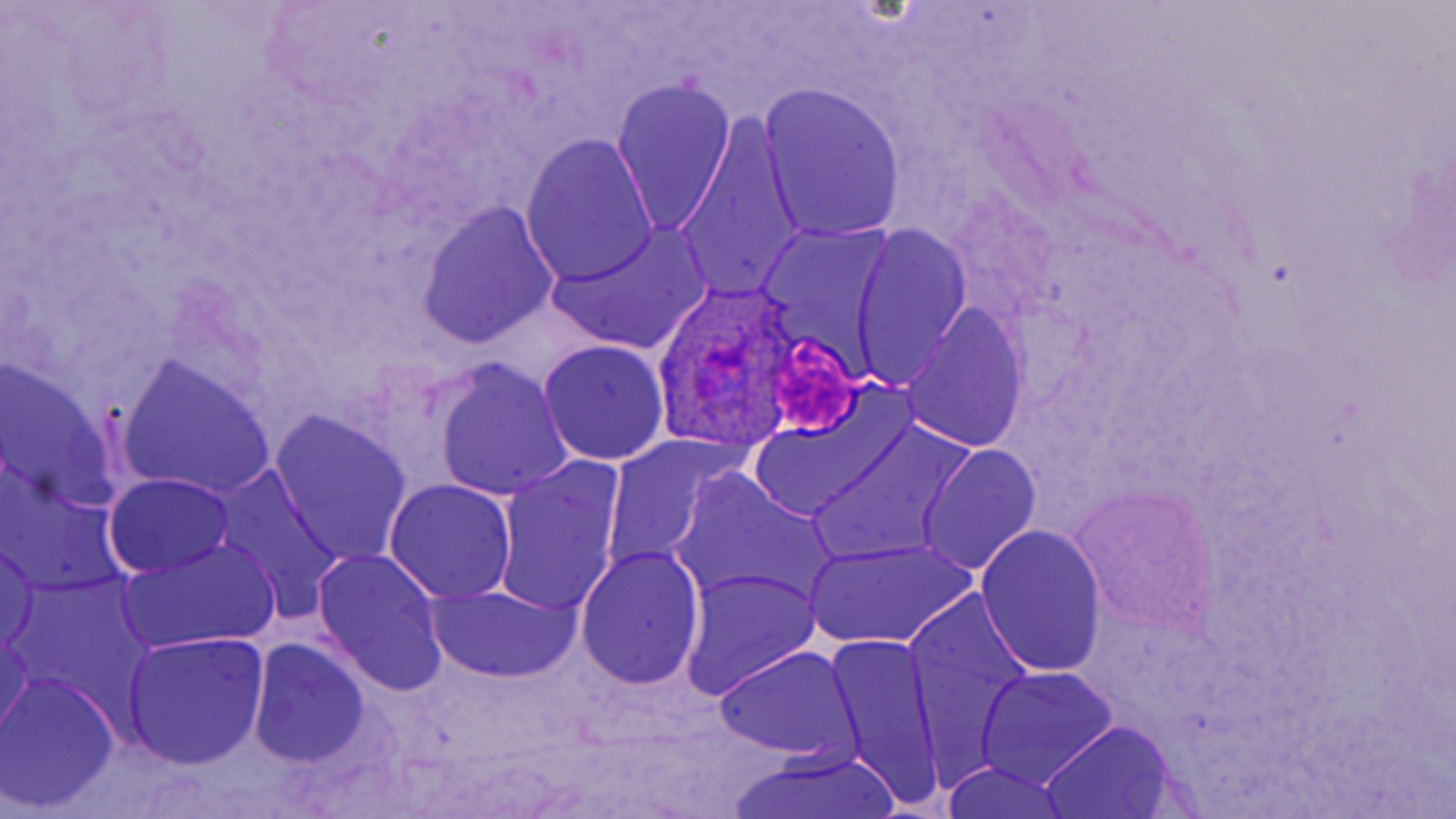

slide-level diagnosis = Plasmodium ovale
modality = optical microscopy
Plasmodium ovale-infected red blood cell locations = approximate bounding boxes as (x1,y1)-(x2,y2) corner pairs in pixels: (657,274)-(807,450)
magnification = 1000x
field of view = one of a larger specimen
image size = 1456×819 pixels
preparation = thin blood smear
platelet locations = approximate bounding boxes as (x1,y1)-(x2,y2) corner pairs in pixels: (771,332)-(860,442)
uninfected red blood cell locations = approximate bounding boxes as (x1,y1)-(x2,y2) corner pairs in pixels: (612,77)-(737,235), (759,83)-(907,244), (672,113)-(806,307), (521,134)-(659,289), (416,202)-(559,347), (545,223)-(710,356), (851,225)-(972,388), (900,305)-(1028,455), (538,340)-(670,464), (0,359)-(125,515), (432,359)-(571,501), (118,360)-(275,499), (744,403)-(901,523), (269,412)-(413,565), (812,421)-(972,565), (599,433)-(739,575), (918,444)-(1040,575), (493,457)-(627,619), (212,467)-(347,617), (672,470)-(840,613), (104,473)-(236,578), (383,478)-(518,603), (1072,487)-(1215,636), (975,523)-(1108,677), (0,538)-(42,655), (806,538)-(976,650), (120,539)-(280,654), (575,544)-(705,692), (311,548)-(450,698), (681,567)-(822,701), (424,583)-(580,684), (905,595)-(1041,783), (0,622)-(33,744), (120,631)-(269,769), (823,633)-(947,811), (248,638)-(372,768), (713,646)-(863,763), (975,667)-(1118,789), (1,671)-(122,812), (1039,722)-(1179,817), (728,746)-(905,819), (939,764)-(1075,819)
stain = May-Grünwald-Giemsa